Look for Plasmodium parasites.
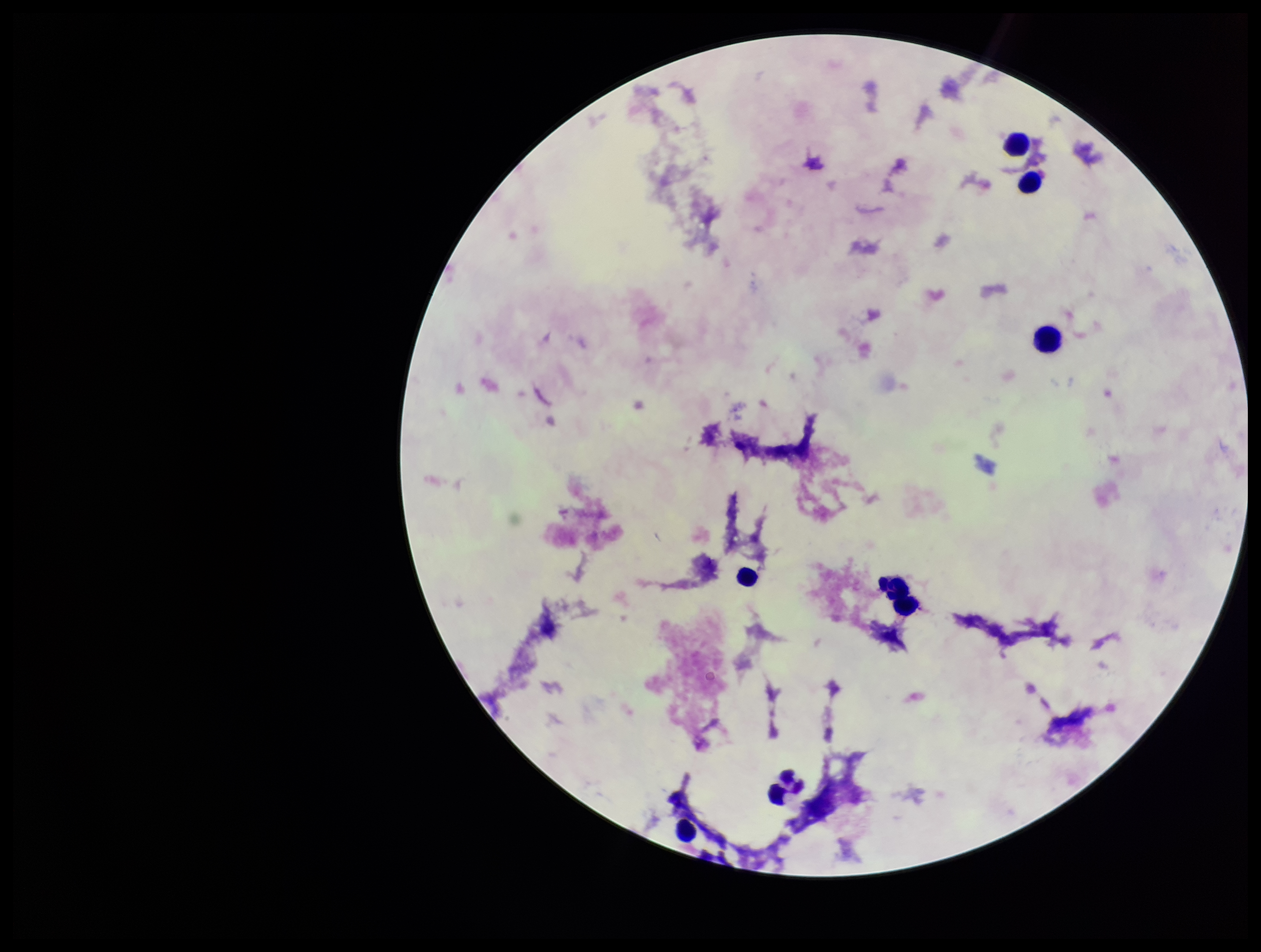
None identified.

capture = smartphone photograph through the microscope eyepiece
field of view = one from this slide
parasite count = 0
image size = 1261×952 pixels
leukocyte count = 7
preparation = thick smear
stain = Giemsa
patient malaria status = negative